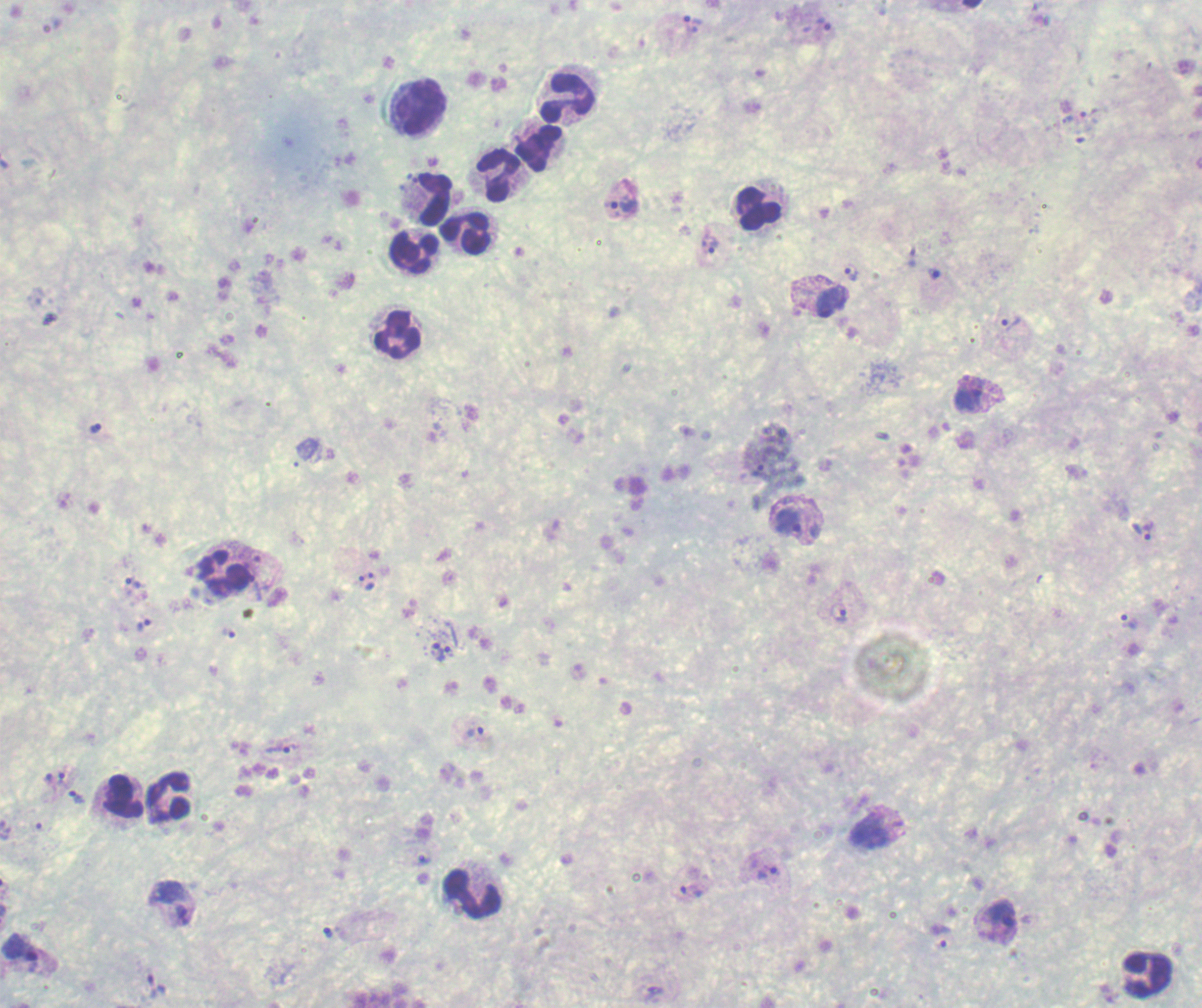

Approximate object centers, in pixels from the top-left corner.
Summary:
  - Leukocyte locations: (x=568, y=98), (x=418, y=107), (x=540, y=149), (x=498, y=174), (x=433, y=200), (x=759, y=209), (x=466, y=232), (x=414, y=252), (x=396, y=334), (x=224, y=575), (x=123, y=797), (x=169, y=797), (x=473, y=894), (x=1148, y=974)
  - Trophozoite locations: (x=693, y=24), (x=820, y=28), (x=1089, y=112), (x=620, y=207), (x=709, y=244), (x=852, y=273), (x=935, y=274), (x=831, y=302), (x=1011, y=324), (x=969, y=398), (x=762, y=465), (x=786, y=520), (x=1145, y=531), (x=263, y=578), (x=361, y=583), (x=371, y=583), (x=134, y=585), (x=839, y=613), (x=1128, y=622), (x=143, y=624), (x=230, y=634), (x=435, y=650), (x=447, y=650), (x=474, y=732), (x=280, y=748), (x=62, y=781), (x=76, y=798), (x=870, y=831), (x=422, y=860), (x=768, y=873), (x=691, y=892), (x=173, y=904), (x=997, y=916), (x=327, y=932), (x=943, y=937), (x=20, y=953), (x=157, y=986)
  - Magnification: 100x
  - Context: previously used in a real diagnosis
  - Field of view: one from this slide
  - Image size: 1202×1008 pixels
  - Background quality: unsatisfactory
  - Preparation: thick smear of blood
  - Stain: Romanowsky
  - Result: positive for Plasmodium parasites